Give a bounding box for every leukocyte visible.
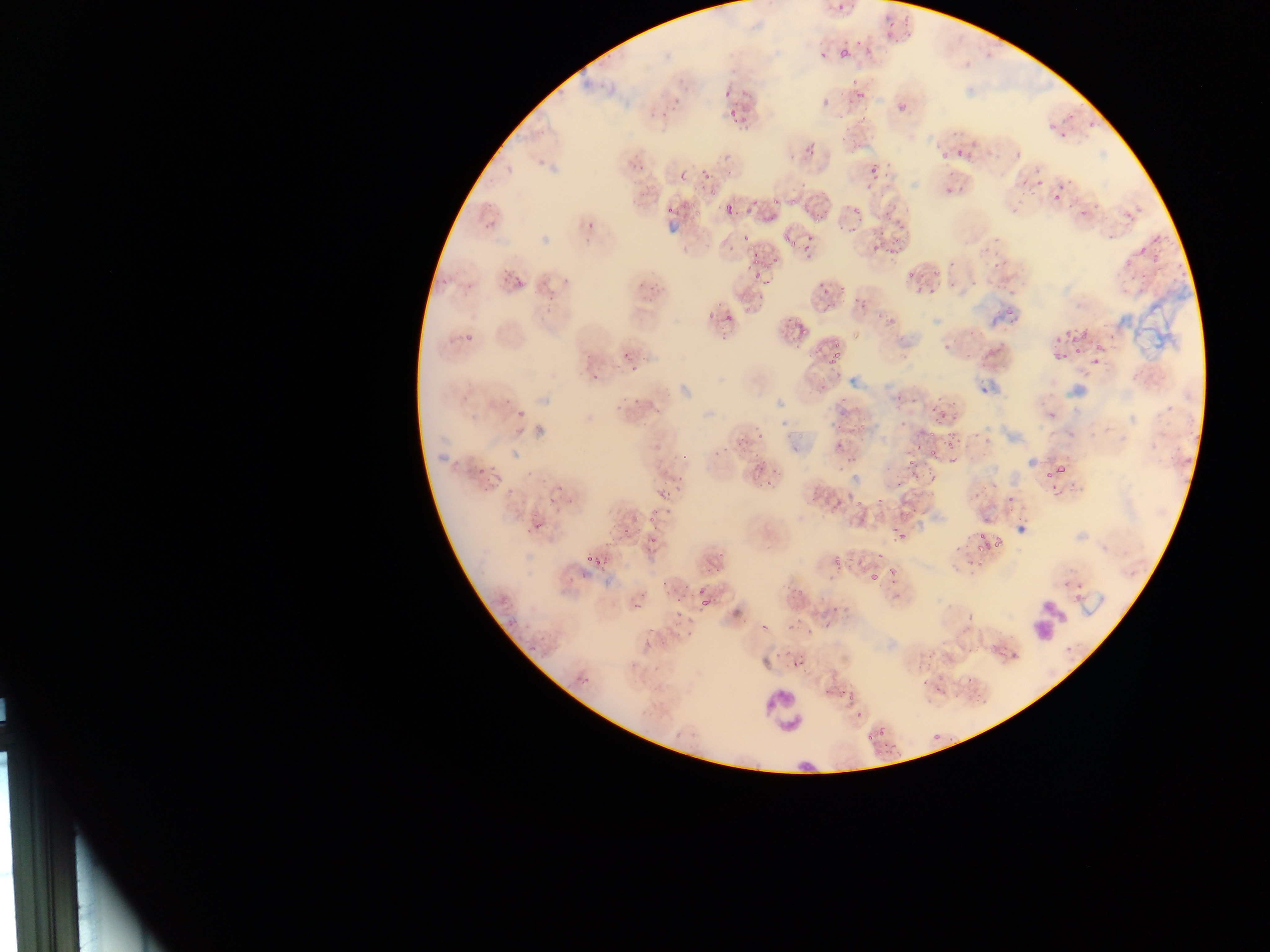
Approximate bounding boxes as [left, top, right, bottom] in pixels.
Leukocytes: [763, 688, 807, 733].

Summary:
  - Malaria parasite locations: [875, 23, 904, 48], [835, 41, 853, 56], [842, 77, 866, 100], [723, 90, 731, 99], [898, 104, 905, 113], [727, 107, 749, 129], [1045, 119, 1068, 136], [936, 137, 962, 163], [799, 143, 816, 159], [694, 160, 714, 188], [863, 162, 880, 187], [943, 172, 969, 191], [1046, 183, 1070, 203], [721, 193, 739, 223], [798, 196, 823, 215], [744, 198, 772, 220], [666, 206, 675, 215], [878, 209, 899, 231], [1122, 209, 1136, 222], [583, 217, 603, 239], [795, 231, 816, 263], [729, 232, 750, 253], [867, 236, 884, 260], [885, 241, 904, 258], [744, 243, 761, 268], [745, 259, 766, 281], [498, 269, 514, 293], [909, 272, 930, 303], [518, 273, 534, 285], [813, 273, 829, 310], [850, 288, 868, 310], [702, 311, 720, 322], [721, 313, 735, 320], [788, 313, 806, 347], [1053, 326, 1088, 342], [1088, 344, 1107, 367], [823, 346, 844, 365], [1049, 348, 1071, 364], [627, 362, 642, 369], [591, 374, 601, 383], [890, 391, 907, 409], [629, 402, 639, 410], [928, 403, 950, 422], [515, 409, 526, 420], [831, 420, 852, 441], [514, 427, 524, 437], [733, 431, 753, 449], [935, 434, 958, 449], [828, 442, 847, 459], [906, 443, 925, 462], [744, 458, 764, 477], [1042, 463, 1070, 481], [927, 469, 941, 485], [651, 484, 669, 498], [831, 499, 842, 509], [532, 515, 550, 531], [642, 515, 658, 521], [892, 531, 911, 543], [649, 537, 656, 547], [863, 540, 888, 558], [975, 541, 994, 558], [840, 552, 861, 572], [585, 554, 596, 565], [825, 555, 836, 567], [864, 569, 881, 579], [695, 584, 703, 593], [888, 584, 902, 596], [675, 596, 686, 606], [627, 598, 642, 607], [727, 600, 748, 624], [675, 612, 683, 620], [756, 613, 774, 639], [823, 616, 841, 628], [781, 618, 806, 635], [990, 632, 1004, 657], [1009, 644, 1020, 660], [787, 659, 804, 670], [918, 672, 932, 685], [842, 683, 864, 703], [867, 722, 886, 737], [927, 727, 943, 738] | approximate [x, y] pixel centers of objects too small to bound: [979, 537]
  - Country: Ghana
  - Preparation: thin blood film
  - Capture: mobile-phone photograph through a microscope
  - Field of view: single
  - Image size: 1270×952 pixels